Report the malaria status of this cell.
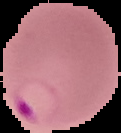

It is parasitized.

From a thin blood smear. Image is 121×133 pixels. Cell region segmented out of the field of view; the surrounding area is masked to black.